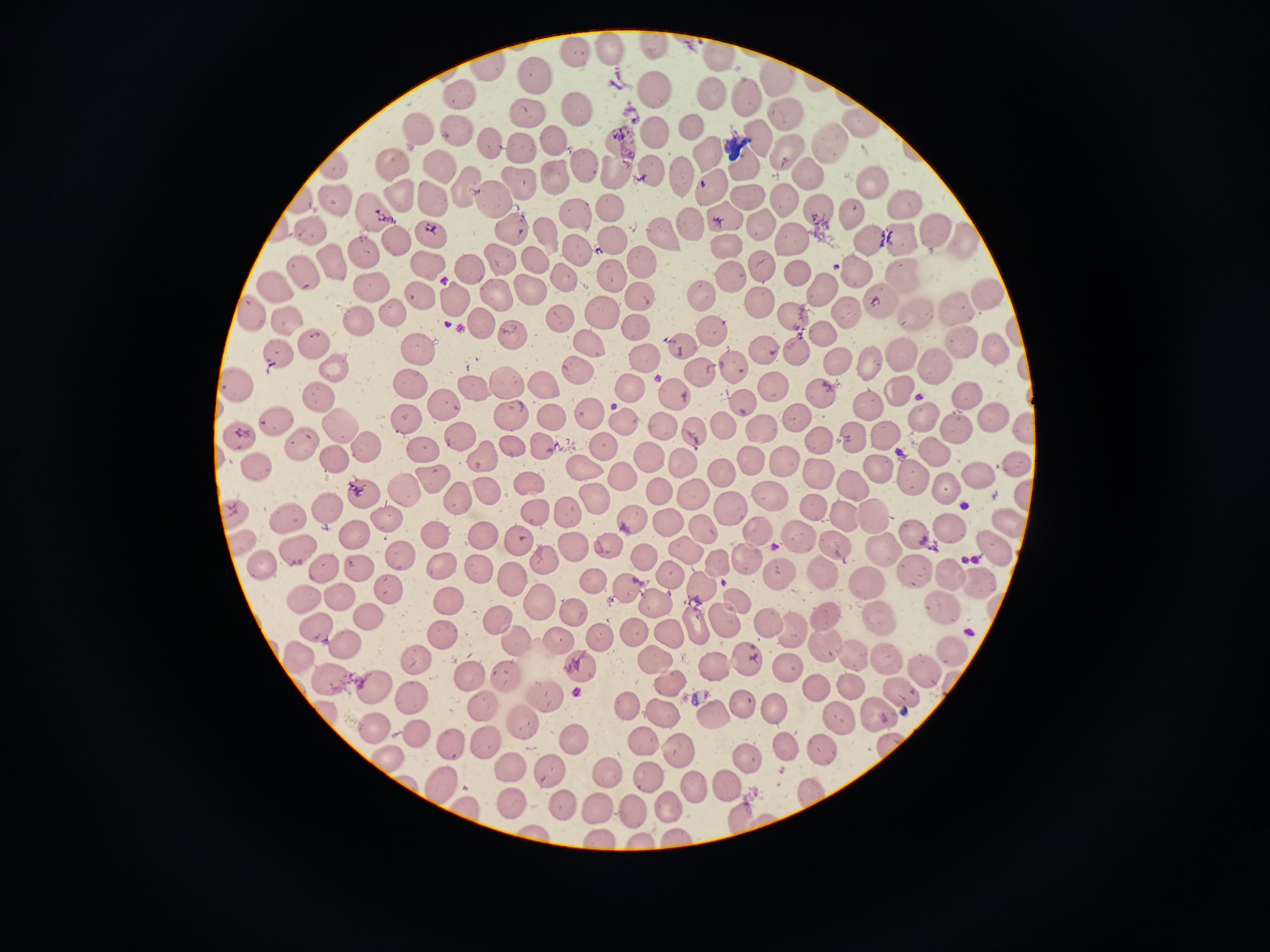

Approximate centers as (x, y) in pixels. Cell locations: (656, 44), (606, 50), (580, 55), (717, 57), (488, 68), (536, 76), (779, 79), (650, 90), (707, 93), (745, 94), (461, 96), (528, 110), (577, 113), (784, 115), (688, 122), (418, 123), (861, 125), (456, 130), (656, 131), (758, 136), (494, 141), (558, 142), (826, 142), (709, 149), (521, 151), (784, 151), (619, 155), (392, 163), (587, 163), (442, 164), (746, 164), (333, 169), (809, 171), (649, 174), (558, 176), (681, 177), (870, 180), (523, 182), (710, 186), (465, 187), (749, 193), (398, 196), (492, 197), (439, 198), (785, 198), (336, 199), (904, 201), (610, 207), (857, 209), (375, 210), (820, 211), (724, 216), (579, 221), (692, 224), (313, 225), (507, 225), (758, 228), (932, 228), (432, 230), (544, 231), (870, 234), (662, 237), (900, 237), (968, 237), (797, 238), (612, 242), (394, 244), (728, 244), (578, 250), (361, 251), (500, 255), (536, 259), (646, 259), (332, 262), (423, 263), (764, 263), (470, 267), (611, 272), (797, 272), (306, 273), (729, 274), (905, 274), (862, 275), (565, 278), (280, 284), (375, 284), (528, 286), (822, 288), (988, 292), (705, 293), (424, 294), (502, 295), (638, 297), (459, 299), (760, 301), (881, 302), (953, 307), (845, 310), (253, 312), (395, 312), (913, 312), (607, 313), (791, 315), (561, 320), (361, 321), (286, 322), (484, 323), (714, 324), (640, 325), (1012, 331), (517, 332), (820, 332), (680, 342), (962, 342), (310, 343), (591, 343), (898, 350), (421, 351), (992, 351), (277, 354), (649, 355), (837, 359), (871, 362), (332, 364), (934, 364), (700, 365), (580, 369), (542, 377), (410, 379), (505, 379), (473, 383), (236, 384), (628, 384), (774, 386), (900, 389), (676, 391), (318, 392), (821, 392), (965, 393), (443, 402), (745, 404), (872, 404), (591, 408), (511, 413), (406, 415), (800, 415), (627, 416), (928, 416), (990, 416), (548, 418), (278, 421), (337, 422), (726, 423), (664, 424), (963, 427), (695, 429), (1024, 429), (759, 430), (888, 433), (463, 434), (242, 436), (821, 436), (857, 437), (605, 443), (365, 444), (509, 444), (300, 446), (425, 446), (547, 450), (933, 450), (650, 455), (330, 456), (750, 456), (485, 458), (681, 463), (786, 463), (1016, 464), (585, 469), (258, 471), (718, 471), (877, 471), (980, 473), (628, 477), (816, 477), (910, 478), (432, 481), (527, 481), (851, 485), (664, 487), (945, 487), (403, 489), (694, 490), (767, 494), (359, 495), (1020, 495), (460, 496), (596, 497), (325, 505), (814, 506), (731, 507), (572, 512), (872, 513), (235, 514), (536, 514), (844, 517), (390, 520), (630, 520), (288, 521), (1008, 521), (673, 523), (701, 527), (758, 528), (948, 529), (438, 533), (483, 534), (914, 535), (519, 536), (357, 538), (802, 540), (835, 542), (240, 544), (609, 545), (993, 547), (573, 549), (688, 549), (291, 551), (884, 553), (401, 554), (644, 557), (547, 558), (748, 559), (319, 564), (719, 564), (442, 566), (913, 567), (264, 568), (360, 568), (477, 568), (777, 572), (670, 573), (824, 573), (953, 573), (590, 579), (512, 580), (980, 580), (868, 583), (624, 586), (700, 586), (387, 589), (339, 595), (304, 599), (448, 599), (654, 601), (742, 601), (535, 604), (937, 605), (576, 610), (821, 614), (497, 616), (367, 617), (878, 617), (694, 623), (766, 623), (725, 624), (317, 631), (442, 632), (789, 632), (671, 634), (558, 637), (599, 637), (512, 638), (343, 640), (822, 646), (950, 650), (293, 652), (654, 653), (854, 657), (886, 658), (750, 662), (417, 663), (578, 667), (788, 667), (719, 668), (927, 670), (329, 675), (507, 675), (473, 677), (669, 684), (848, 685), (370, 688), (814, 688), (900, 690), (408, 692), (543, 693), (622, 699), (745, 699), (483, 700), (773, 705), (662, 708), (713, 710), (875, 712), (839, 717), (525, 723), (373, 725), (420, 734), (567, 734), (486, 738), (643, 738), (452, 744), (678, 746), (788, 746), (891, 747), (825, 748), (747, 756), (384, 761), (514, 765), (609, 770), (551, 771), (650, 772), (732, 784), (439, 785), (699, 790), (811, 795), (669, 804), (509, 805), (561, 806), (632, 806), (598, 807), (463, 810), (741, 817), (763, 821). Photographed with a smartphone camera at the microscope eyepiece. One field from this slide. Thin blood smear. Giemsa stain. Image is 1270×952 pixels.